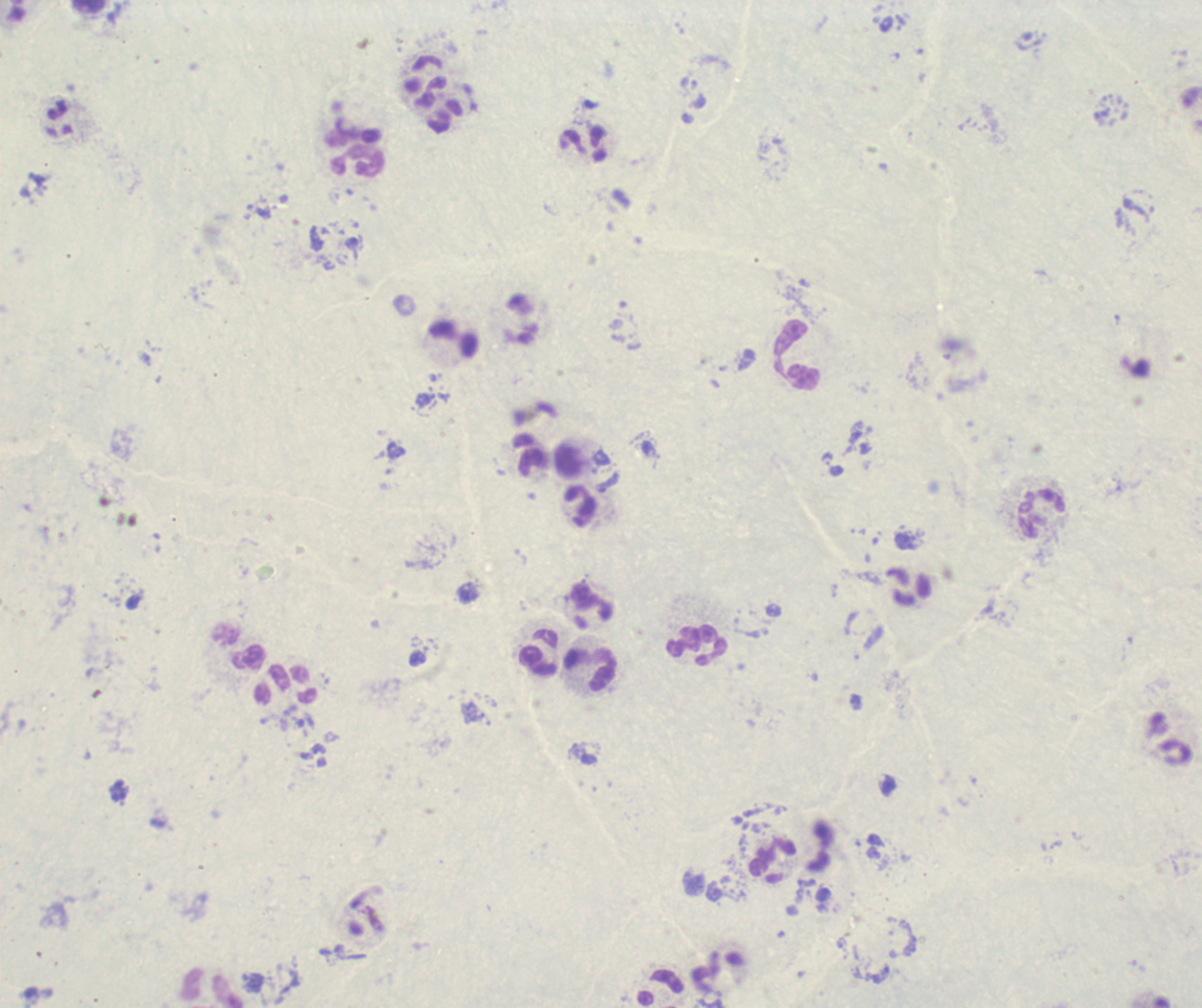 Approximate centers as {x, y} in pixels. Leukocyte locations: {357, 162}, {452, 338}, {797, 354}, {579, 505}, {1041, 513}, {699, 645}, {540, 654}, {589, 671}, {285, 683}, {772, 858}. Previously used in a real diagnosis. Result: negative for Plasmodium parasites. One field from this slide. Romanowsky-stained preparation. Background quality: poor. Image is 1202×1008 pixels. Thick blood smear. 100x magnification.